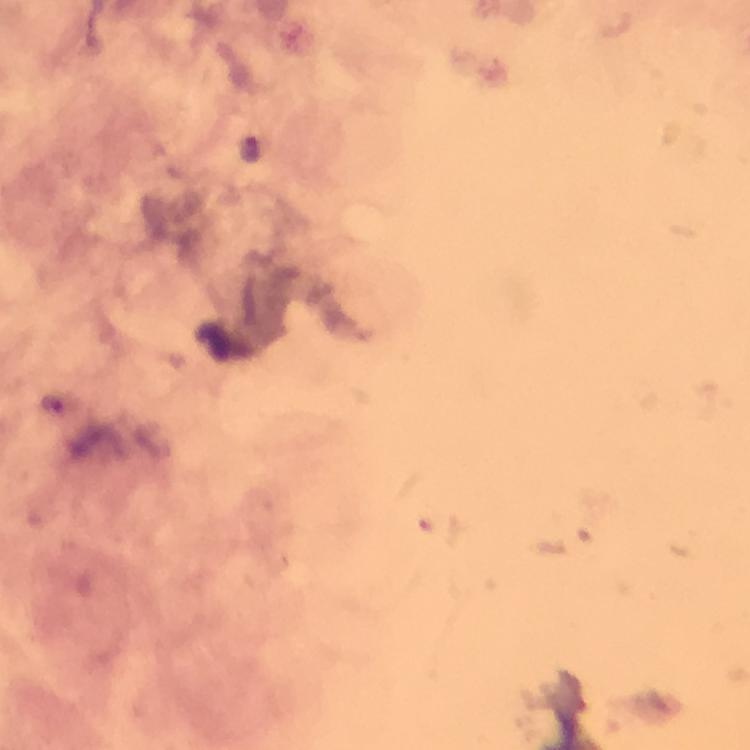 Approximate centers as {x, y} in pixels. Plasmodium parasite locations: {248, 148}. Giemsa-stained preparation. From a diagnostic examination for malaria. Image is 750×750 pixels. 100x magnification. Immersion oil was used. Thick blood smear. A crop from one field of view. Photographed through the microscope with a smartphone camera.